Locate every parasitized red blood cell.
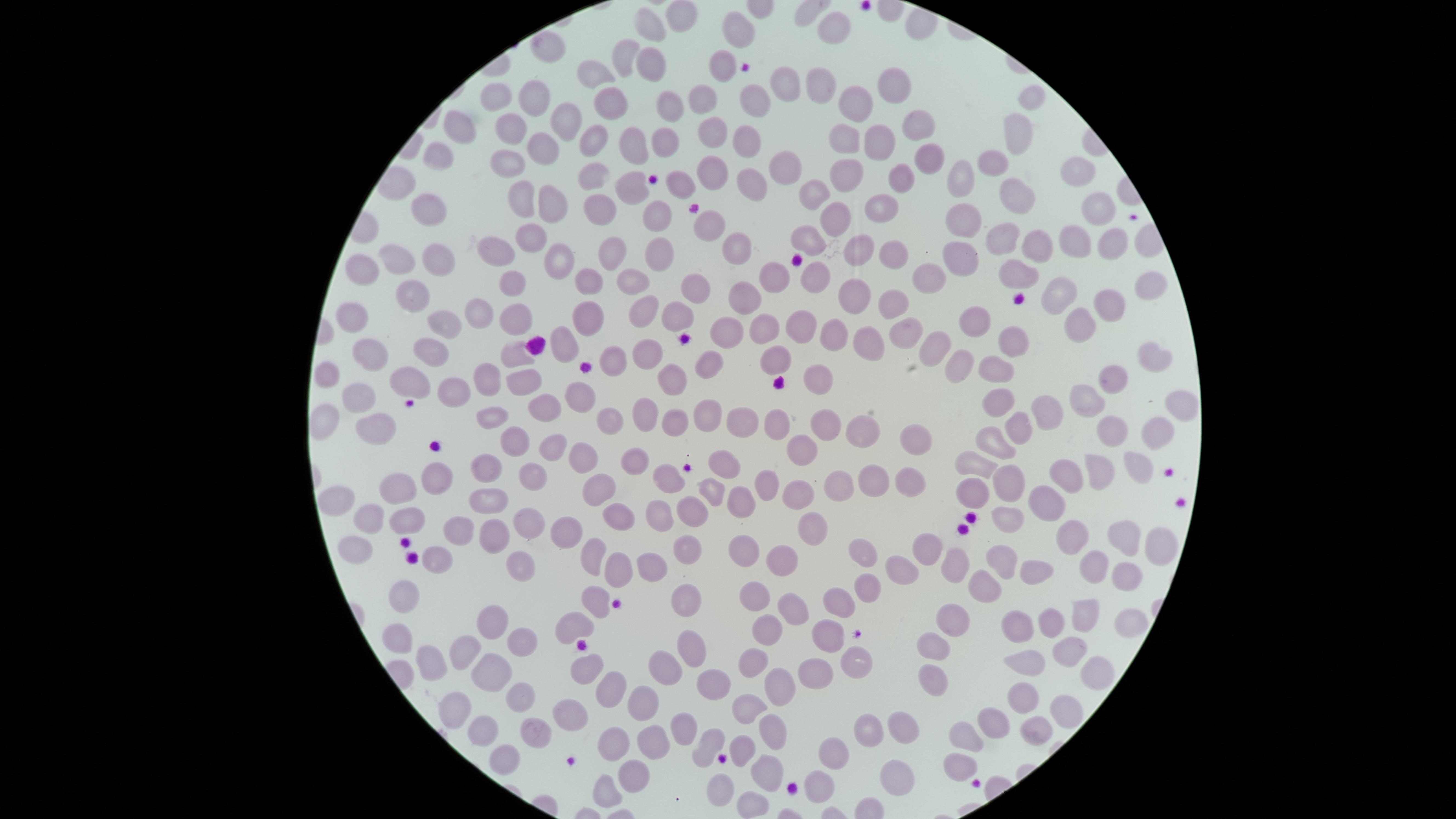
No parasitized red blood cells identified.

Approximate marker points as (x, y) in pixels.
Summary:
  - Uninfected red blood cells: (680, 19), (647, 24), (836, 31), (740, 32), (545, 46), (628, 55), (651, 65), (724, 67), (596, 75), (781, 87), (893, 88), (823, 90), (494, 97), (1030, 97), (533, 101), (757, 103), (855, 104), (707, 105), (612, 107), (661, 107), (916, 120), (559, 121), (518, 127), (457, 129), (713, 130), (667, 135), (1014, 135), (593, 139), (845, 139), (745, 140), (879, 140), (634, 147), (535, 148), (930, 159), (437, 162), (995, 164), (780, 165), (510, 166), (593, 174), (713, 174), (964, 175), (1077, 175), (847, 176), (901, 178), (750, 182), (631, 187), (1013, 190), (816, 194), (522, 201), (548, 206), (598, 207), (880, 208), (1098, 208), (432, 212), (832, 217), (961, 217), (656, 219), (709, 224), (531, 235), (1070, 236), (811, 237), (1005, 238), (1111, 238), (1036, 244), (734, 248), (863, 250), (500, 252), (610, 253), (888, 253), (436, 255), (658, 255), (961, 255), (397, 257), (554, 262), (359, 270), (932, 272), (1017, 273), (774, 278), (632, 281), (585, 283), (819, 283), (1154, 283), (512, 288), (698, 289), (1057, 289), (745, 291), (409, 294), (856, 296), (892, 298), (1108, 298), (678, 310), (644, 312), (476, 314), (516, 318), (582, 320), (973, 321), (356, 323), (803, 325), (442, 326), (769, 326), (1080, 326), (729, 329), (904, 334), (839, 338), (866, 339), (1008, 339), (565, 344), (931, 345), (371, 352), (648, 352), (1151, 352), (431, 353), (515, 354), (782, 357), (613, 361), (958, 364), (998, 365), (707, 366), (331, 373), (485, 376), (1117, 377), (824, 379), (411, 380), (522, 380), (674, 380), (452, 388), (580, 390), (359, 397), (1180, 398), (1090, 399), (1000, 400), (542, 404), (1055, 408), (710, 415), (644, 417), (740, 417), (606, 418), (494, 421), (675, 422), (829, 424), (782, 425), (375, 428), (1017, 428), (865, 431), (1158, 431), (1116, 433), (918, 438), (512, 441), (993, 443), (549, 445), (803, 450), (583, 458), (638, 459), (486, 462), (721, 462), (974, 465), (1136, 468), (1102, 469), (531, 474), (1070, 476), (665, 478), (1004, 480), (767, 482), (872, 482), (911, 482), (432, 483), (595, 484), (839, 485), (712, 489), (395, 490), (797, 492), (973, 493), (743, 498), (1049, 500), (340, 502), (486, 502), (658, 509), (694, 514), (372, 516), (616, 517), (403, 523), (1006, 523), (524, 526), (810, 528), (454, 530), (566, 532), (490, 535), (1122, 535), (1077, 536), (1155, 541), (929, 543), (691, 544), (358, 547), (747, 548), (859, 550), (594, 553), (433, 556), (782, 556), (1003, 562), (954, 565), (1091, 565), (512, 567), (655, 567), (614, 568), (1036, 571), (1130, 573), (906, 574), (980, 588), (403, 589), (869, 589), (754, 594), (678, 597), (594, 600), (789, 604), (841, 606), (1085, 613), (493, 618), (1123, 618), (952, 619), (1055, 619), (1022, 625), (573, 627), (400, 629), (772, 630), (829, 638), (523, 640), (935, 646), (691, 647), (1070, 649), (463, 655), (757, 656), (1025, 657), (852, 661), (431, 662), (667, 664), (495, 665), (583, 667), (818, 673), (1091, 675), (931, 680), (710, 681), (779, 686), (605, 689), (517, 690), (1018, 698), (644, 706), (751, 709), (1065, 710), (457, 711), (571, 711), (996, 721), (686, 725), (905, 728), (1036, 728), (481, 732), (535, 732), (772, 732), (865, 733), (969, 737), (652, 742), (613, 744), (700, 745), (741, 749), (835, 751), (501, 757), (959, 763), (763, 764), (629, 773), (894, 776), (821, 782), (602, 792), (722, 792), (753, 799)
  - Field of view: single
  - Image size: 1456×819 pixels
  - Capture: smartphone photograph through the microscope eyepiece
  - Stain: Giemsa
  - Preparation: thin smear of blood
  - Visible region: circular